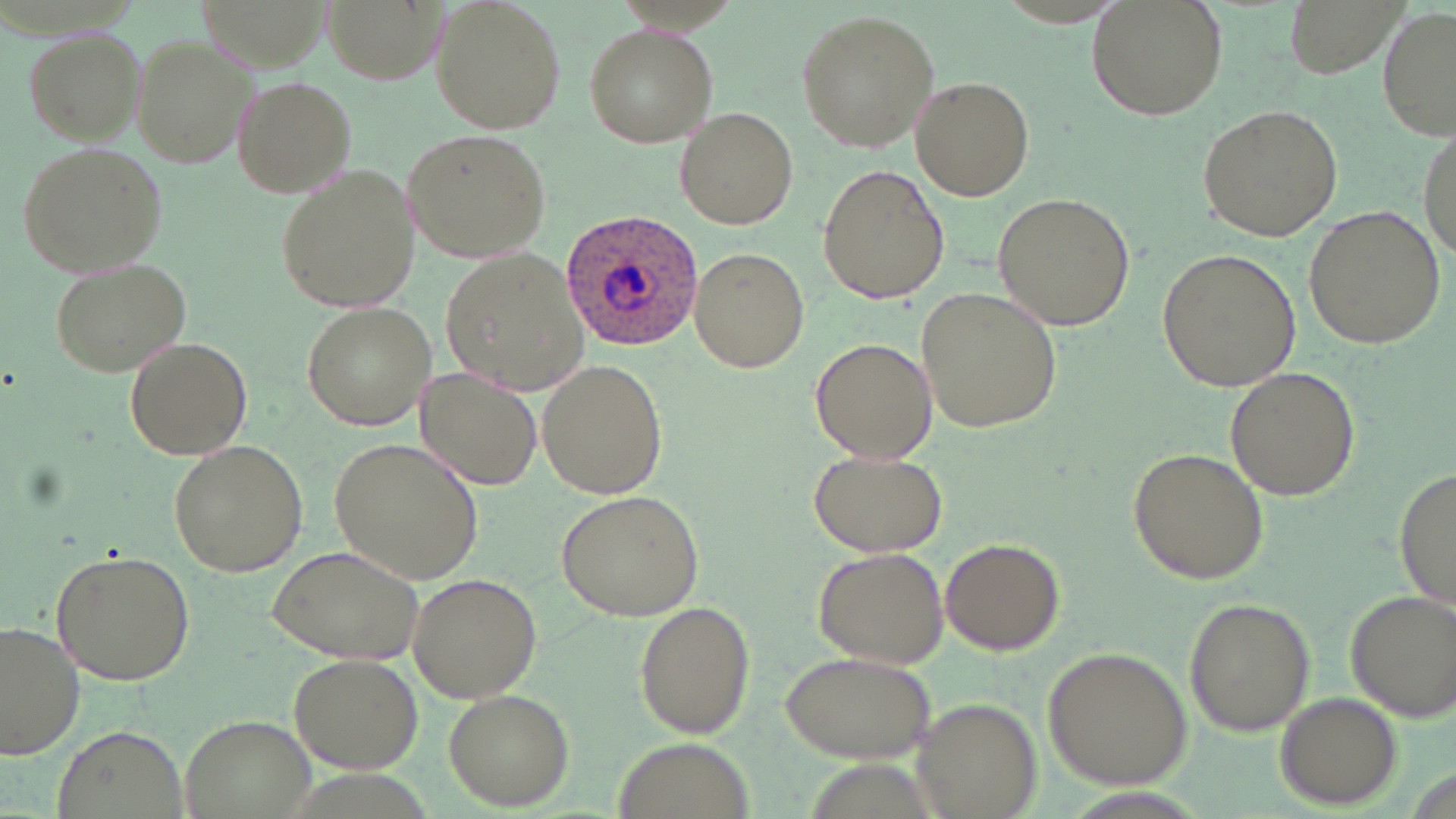
Summary:
  - Coordinate format: approximate bounding boxes as (x1,y1)-(x2,y2) corner pairs in pixels
  - Uninfected red blood cell locations: (429,0)-(566,134), (1085,0)-(1227,118), (1378,5)-(1454,144), (798,12)-(940,151), (583,23)-(718,146), (24,26)-(149,144), (129,32)-(258,172), (230,73)-(359,196), (910,73)-(1036,201), (1196,105)-(1345,242), (673,108)-(799,230), (1417,125)-(1454,267), (400,129)-(553,262), (14,139)-(168,277), (274,166)-(419,312), (816,166)-(950,304), (992,192)-(1136,331), (1303,205)-(1447,349), (439,247)-(593,398), (688,248)-(810,373), (1158,248)-(1301,392), (47,256)-(192,377), (920,286)-(1064,433), (300,302)-(438,430), (121,336)-(254,461), (811,337)-(937,466), (534,357)-(668,502), (1225,365)-(1359,503), (415,366)-(545,493), (329,435)-(486,585), (166,439)-(308,578), (1127,448)-(1269,585), (808,449)-(947,558), (1393,462)-(1455,614), (555,489)-(704,620), (940,537)-(1065,655), (265,544)-(428,664), (812,546)-(951,669), (48,549)-(194,686), (404,573)-(544,702), (1340,588)-(1454,722), (1182,596)-(1315,736), (632,598)-(755,736), (0,618)-(85,766), (1044,646)-(1193,788), (776,649)-(938,762), (289,652)-(420,773), (442,687)-(572,808), (1275,693)-(1401,808), (912,699)-(1040,818), (180,713)-(317,819), (50,725)-(191,819), (607,740)-(760,817)
  - Plasmodium ovale-infected red blood cell locations: (559,208)-(703,351)
  - Slide-level diagnosis: Plasmodium ovale
  - Image size: 1456×819 pixels
  - Field of view: single
  - Preparation: thin blood smear
  - Modality: optical microscopy
  - Stain: May-Grünwald-Giemsa
  - Magnification: 1000x